Describe the morphology of the erythrocytes.
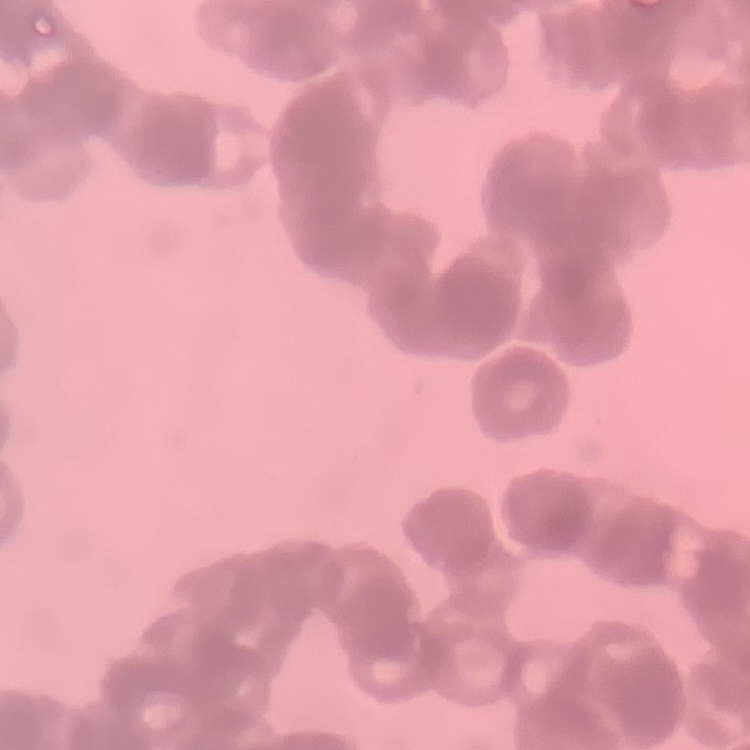
They show rouleaux formation.

image_type: one tile cut from a larger photomicrograph
preparation: thin blood smear
stain: Field's or Giemsa